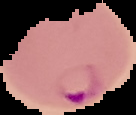
image type = cell region segmented out of the field of view; surrounding area masked to black
malaria status = parasitized
image size = 136×115 pixels
preparation = thin blood film